Report the malaria status of this cell.
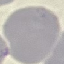
It is uninfected.

Summary:
  - Preparation: thin blood smear
  - Image type: automatically extracted cell patch, resized to 64 × 64 pixels
  - Stain: Giemsa
  - Capture: smartphone camera at the microscope eyepiece